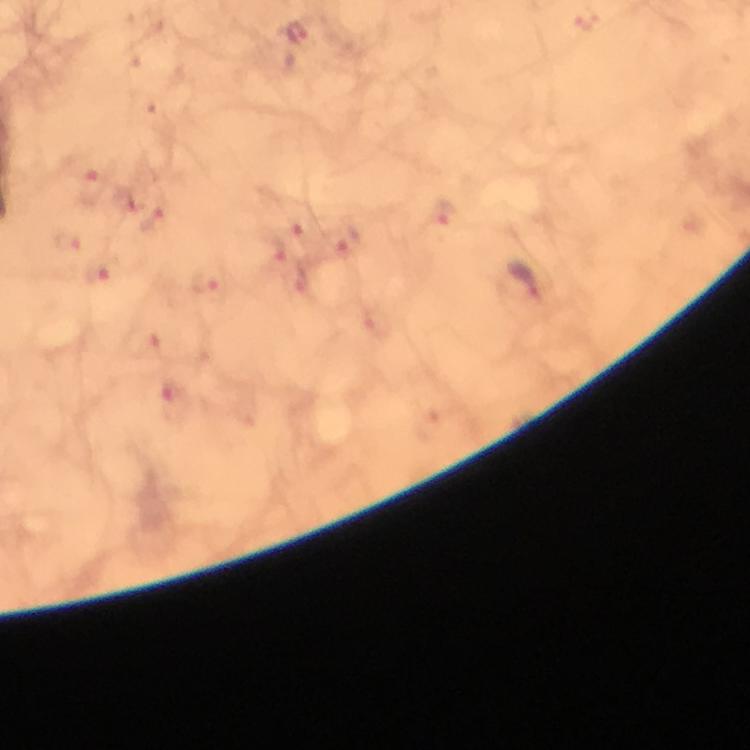
{
  "cropped_from": "a single field of view",
  "image_size": "750×750 pixels",
  "magnification": "100x",
  "preparation": "thick blood film",
  "plasmodium_parasite_locations": "approximate centers as (x, y) in pixels: (587, 18), (297, 34), (94, 188), (124, 201), (445, 219), (151, 222), (299, 225), (343, 240), (68, 241), (272, 252), (102, 272), (523, 281), (201, 282), (141, 343), (171, 401)",
  "context": "from a malaria diagnostic workup",
  "capture": "smartphone mounted on the microscope",
  "stain": "Giemsa",
  "immersion_oil": "applied"
}